Assess this cell for malaria.
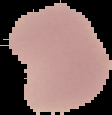

Uninfected.

Summary:
  - Image type: segmented cell region on a black background
  - Image size: 112×115 pixels
  - Preparation: thin blood film